Identify the preparation type.
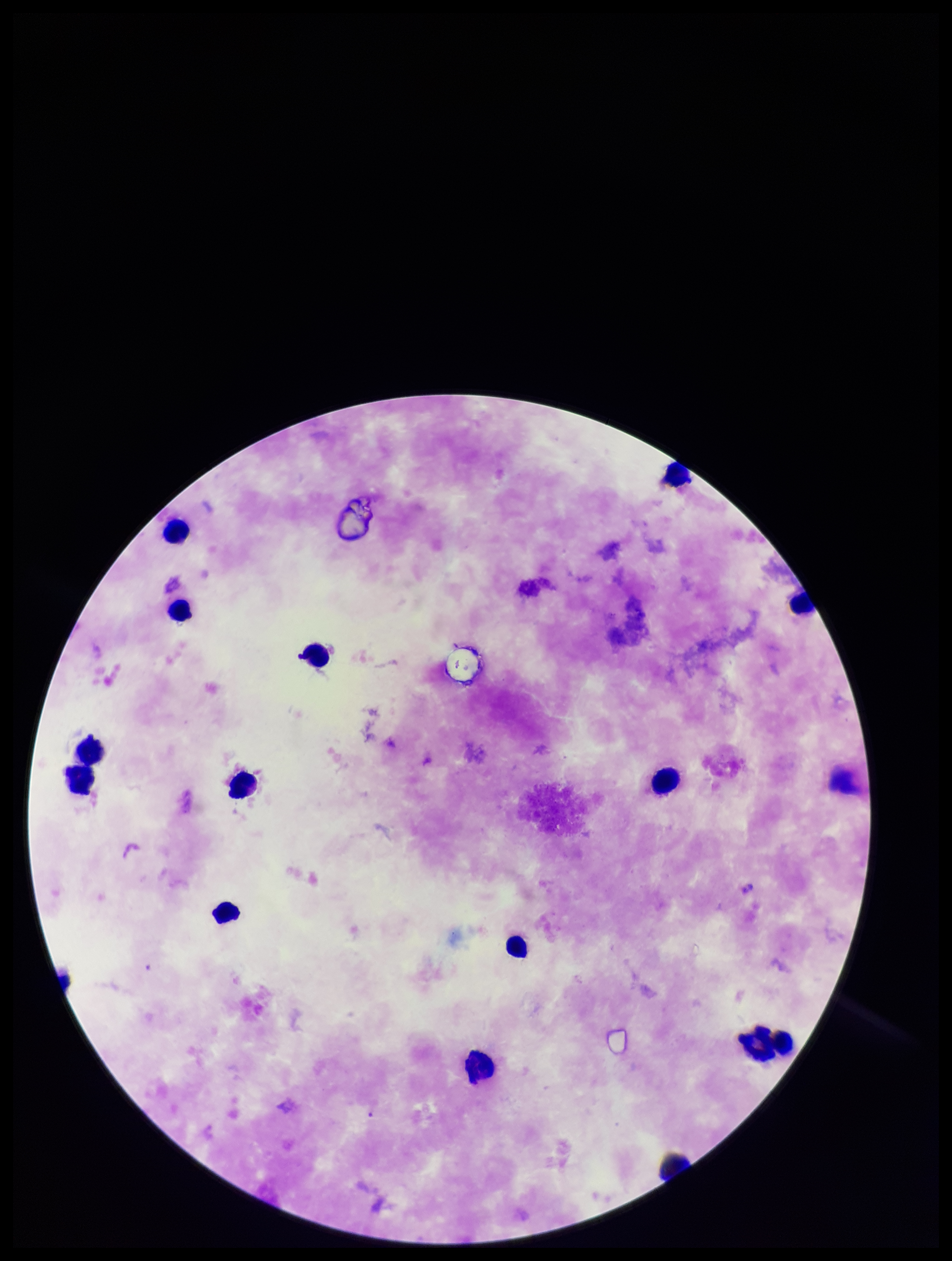
Thick.

Giemsa stain. Single field of view. Parasite count: 0. Plasmodium parasites: none identified. Leukocyte count: 15. Patient malaria status: negative. Smartphone photograph taken through the eyepiece of a microscope. Image is 952×1261 pixels.